Classify this cell by malaria status.
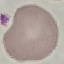

It is uninfected.

Summary:
  - Preparation: thin blood smear
  - Image type: cell patch, automatically extracted from a larger field of view and resized to 64 × 64 pixels
  - Stain: Giemsa
  - Capture: smartphone camera at the microscope eyepiece